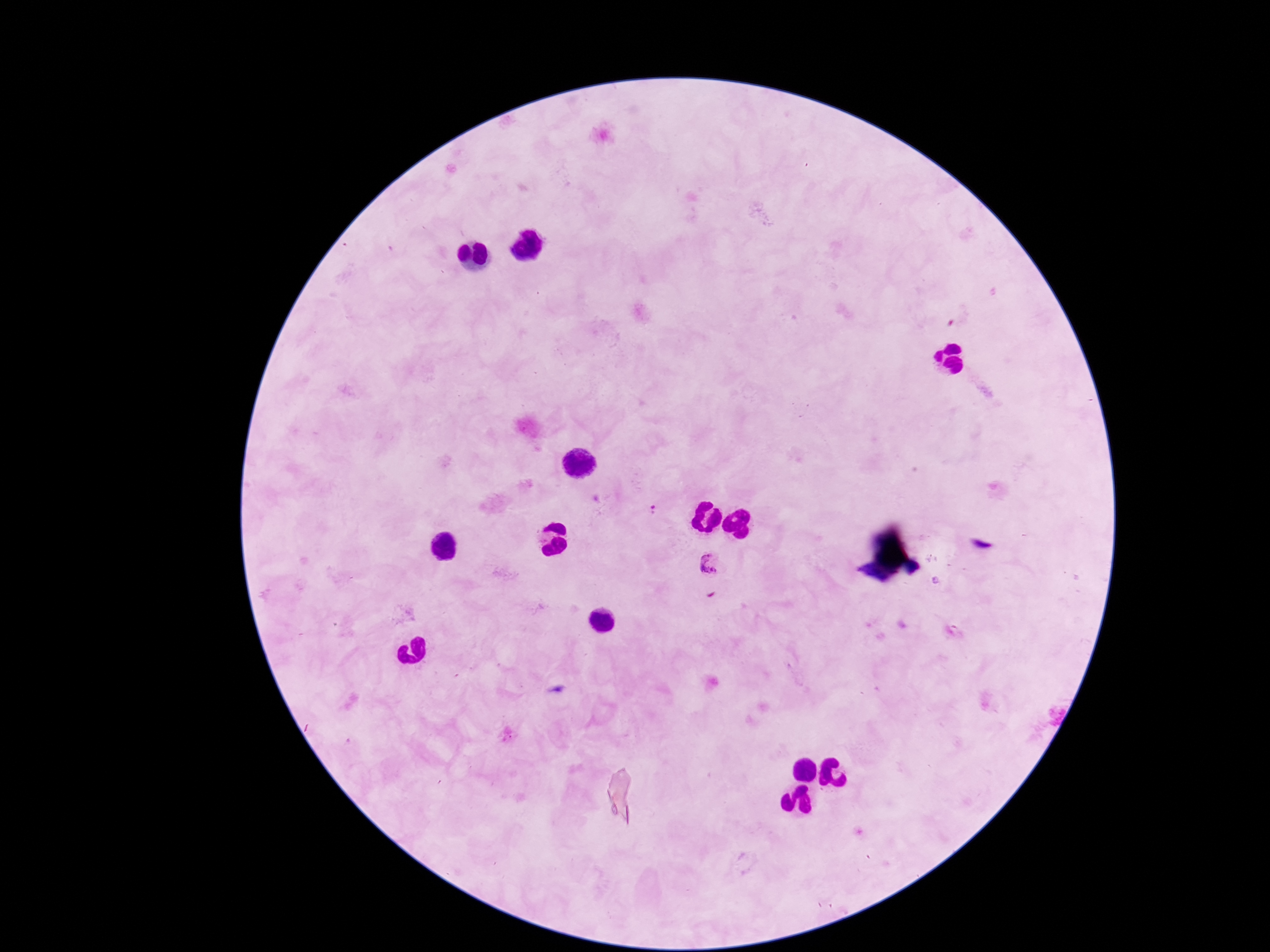

Approximate object centers, in pixels from the top-left corner.
Summary:
  - Plasmodium parasite locations: (x=654, y=511), (x=709, y=561)
  - Magnification: 100x
  - Image size: 1270×952 pixels
  - Field of view: one from this slide
  - Stain: Giemsa
  - Capture: smartphone camera through the microscope eyepiece
  - Preparation: thick blood smear
  - Patient malaria status: infected